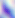

Toxoplasma gondii is shown. 400x magnification. Micrograph.